Locate and identify every blood parasite.
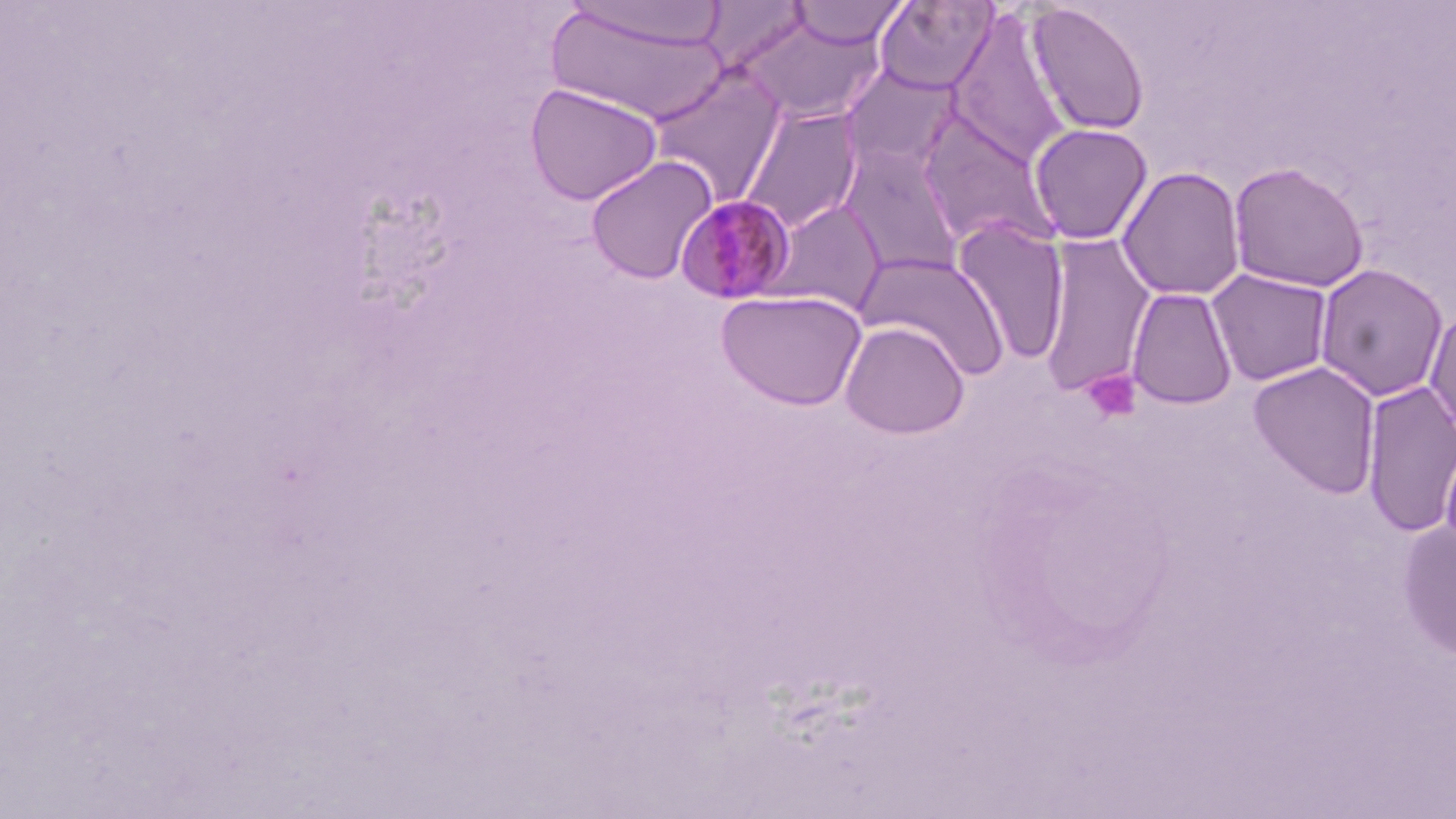

Approximate bounding boxes as named x1/y1/x2/y2 corners in pixels.
Plasmodium malariae-infected red blood cells: (x1=674, y1=195, x2=797, y2=307).
No Plasmodium falciparum, Plasmodium ovale, Plasmodium vivax, Babesia divergens, or Trypanosoma brucei observed.

Platelet locations: (x1=1082, y1=369, x2=1142, y2=424). Uninfected red blood cell locations: (x1=563, y1=0, x2=728, y2=51), (x1=874, y1=0, x2=998, y2=95), (x1=788, y1=1, x2=908, y2=49), (x1=698, y1=2, x2=812, y2=72), (x1=1026, y1=3, x2=1151, y2=137), (x1=545, y1=6, x2=729, y2=124), (x1=947, y1=10, x2=1072, y2=166), (x1=737, y1=14, x2=885, y2=124), (x1=645, y1=63, x2=788, y2=207), (x1=840, y1=64, x2=963, y2=175), (x1=524, y1=82, x2=663, y2=206), (x1=739, y1=105, x2=864, y2=233), (x1=914, y1=110, x2=1062, y2=252), (x1=1028, y1=122, x2=1154, y2=245), (x1=836, y1=143, x2=965, y2=279), (x1=586, y1=156, x2=719, y2=285), (x1=1228, y1=160, x2=1370, y2=293), (x1=1117, y1=166, x2=1246, y2=302), (x1=764, y1=199, x2=887, y2=316), (x1=952, y1=220, x2=1071, y2=367), (x1=1038, y1=235, x2=1156, y2=396), (x1=853, y1=251, x2=1010, y2=379), (x1=1313, y1=263, x2=1450, y2=402), (x1=1205, y1=269, x2=1335, y2=387), (x1=1126, y1=287, x2=1238, y2=410), (x1=715, y1=289, x2=867, y2=411), (x1=1423, y1=302, x2=1456, y2=444), (x1=838, y1=320, x2=970, y2=439), (x1=1248, y1=361, x2=1382, y2=498), (x1=1360, y1=381, x2=1456, y2=539), (x1=1439, y1=431, x2=1456, y2=565), (x1=1395, y1=518, x2=1456, y2=660). Slide-level diagnosis: Plasmodium malariae. Image is 1456×819 pixels. Captured at 1000x magnification. One field of a larger specimen. May-Grünwald-Giemsa-stained preparation. Thin blood film. Optical microscopy.